Identify the preparation type.
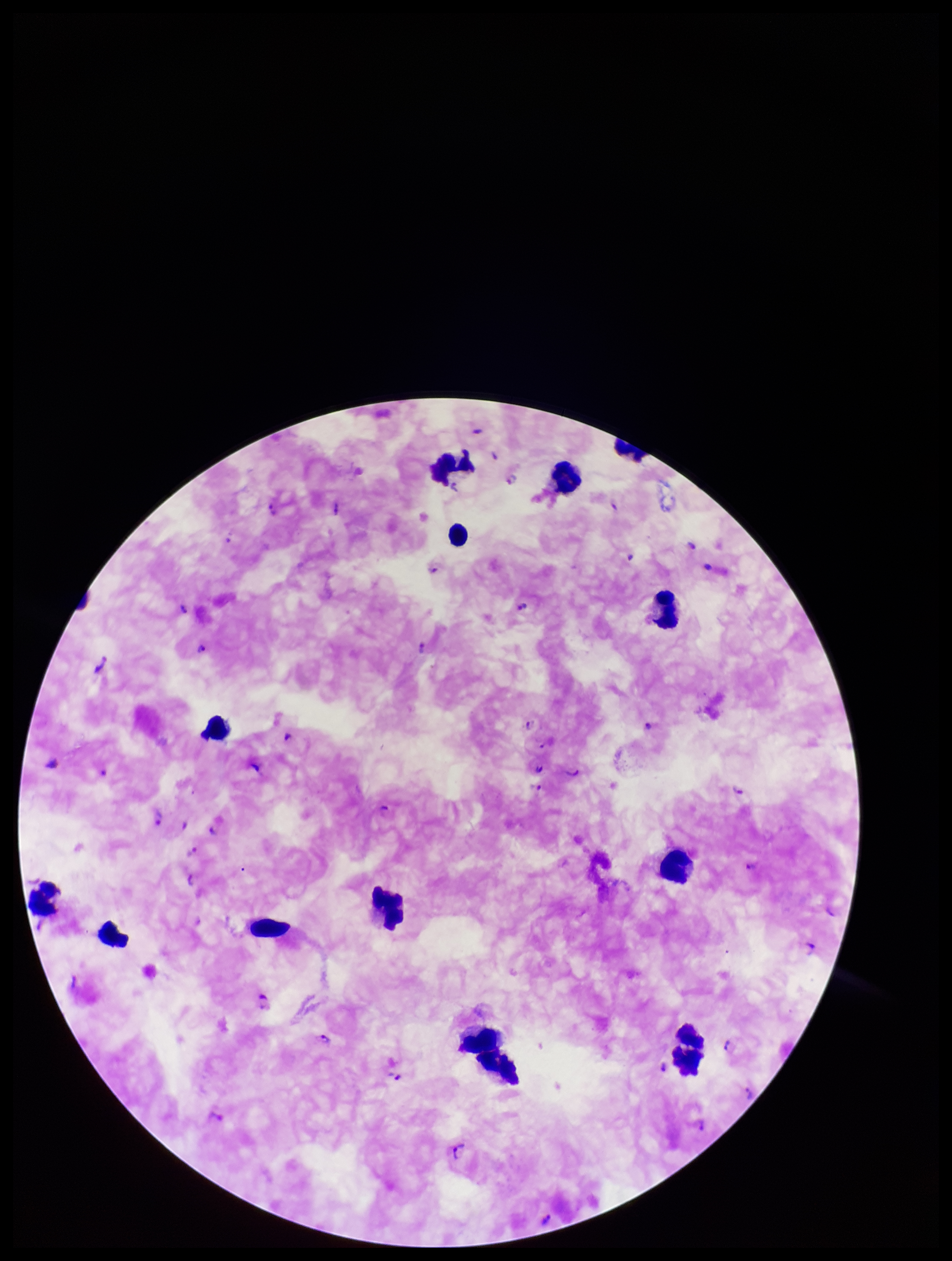

It is a thick blood smear.

Summary:
  - Field of view: single
  - Plasmodium parasites: identified
  - Leukocyte count: 13
  - Parasite count: 25
  - Capture: smartphone photograph through the microscope eyepiece
  - Stain: Giemsa
  - Species reported for this patient: Plasmodium falciparum
  - Patient malaria status: infected
  - Image size: 952×1261 pixels